Locate and identify every blood parasite.
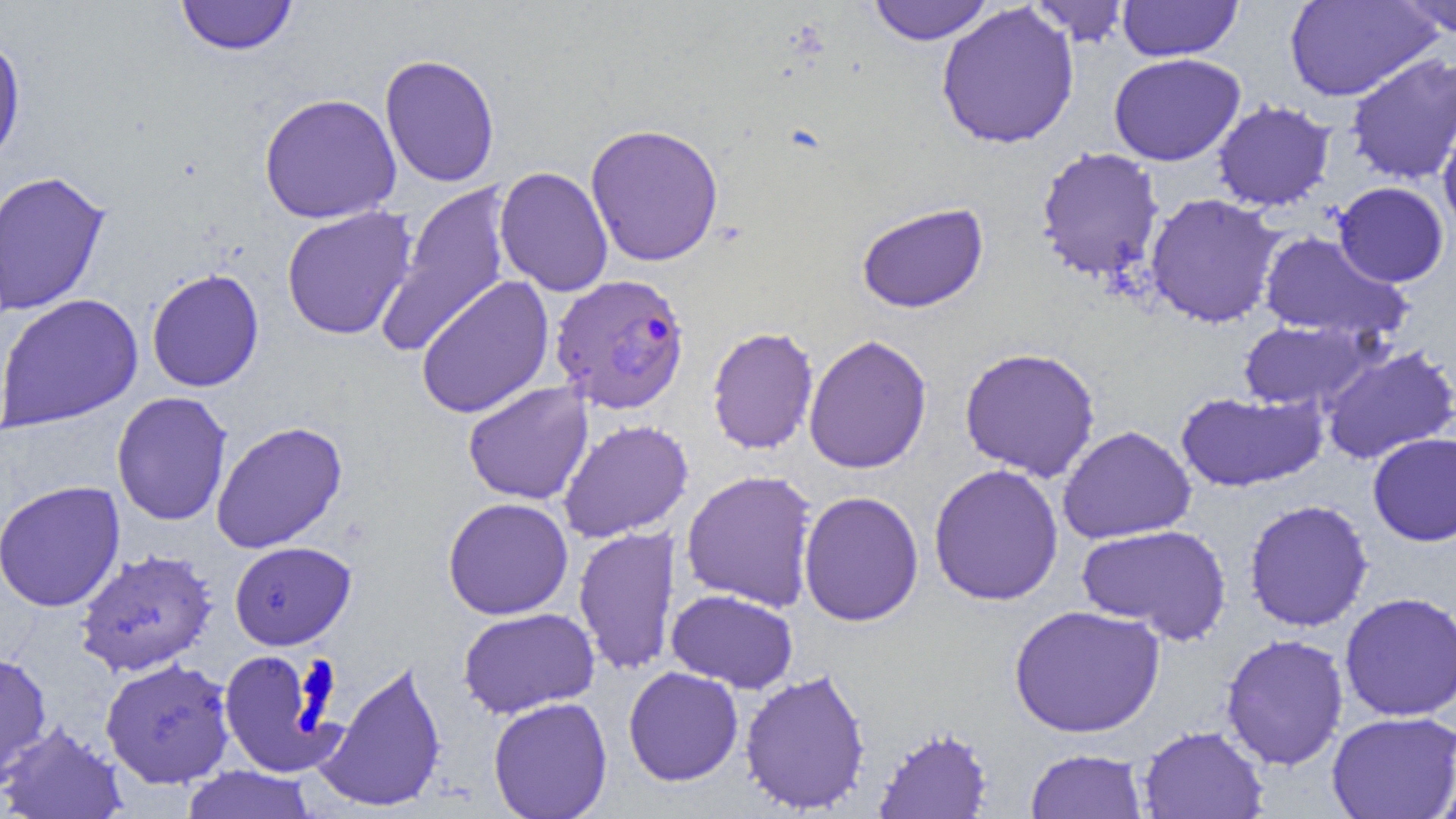
Approximate bounding boxes as named x1/y1/x2/y2 corners in pixels.
Plasmodium falciparum-infected red blood cells: (x1=549, y1=273, x2=690, y2=415).
No Plasmodium ovale, Plasmodium malariae, Plasmodium vivax, Babesia divergens, or Trypanosoma brucei observed.

Uninfected red blood cell locations: (x1=175, y1=0, x2=297, y2=56), (x1=1027, y1=0, x2=1132, y2=46), (x1=1285, y1=0, x2=1441, y2=102), (x1=1396, y1=0, x2=1456, y2=38), (x1=867, y1=1, x2=994, y2=45), (x1=1117, y1=1, x2=1242, y2=61), (x1=935, y1=3, x2=1080, y2=150), (x1=0, y1=33, x2=26, y2=169), (x1=1345, y1=52, x2=1456, y2=186), (x1=379, y1=53, x2=501, y2=187), (x1=1108, y1=53, x2=1245, y2=166), (x1=259, y1=92, x2=402, y2=225), (x1=1212, y1=101, x2=1335, y2=212), (x1=1437, y1=108, x2=1455, y2=239), (x1=585, y1=123, x2=724, y2=267), (x1=1035, y1=147, x2=1165, y2=282), (x1=495, y1=165, x2=614, y2=297), (x1=0, y1=169, x2=112, y2=317), (x1=379, y1=181, x2=513, y2=357), (x1=1333, y1=181, x2=1449, y2=287), (x1=1145, y1=193, x2=1284, y2=328), (x1=856, y1=202, x2=989, y2=314), (x1=280, y1=206, x2=418, y2=341), (x1=1257, y1=231, x2=1411, y2=342), (x1=146, y1=268, x2=265, y2=392), (x1=415, y1=274, x2=555, y2=420), (x1=0, y1=293, x2=144, y2=432), (x1=1238, y1=319, x2=1377, y2=411), (x1=706, y1=326, x2=819, y2=455), (x1=802, y1=334, x2=933, y2=474), (x1=1319, y1=345, x2=1456, y2=465), (x1=959, y1=347, x2=1101, y2=482), (x1=462, y1=381, x2=593, y2=505), (x1=1175, y1=390, x2=1328, y2=493), (x1=112, y1=392, x2=232, y2=526), (x1=558, y1=419, x2=694, y2=542), (x1=211, y1=421, x2=348, y2=553), (x1=1057, y1=425, x2=1196, y2=544), (x1=1367, y1=432, x2=1456, y2=546), (x1=928, y1=463, x2=1064, y2=606), (x1=681, y1=469, x2=819, y2=611), (x1=0, y1=480, x2=126, y2=612), (x1=798, y1=490, x2=924, y2=627), (x1=442, y1=497, x2=574, y2=620), (x1=1243, y1=499, x2=1374, y2=632), (x1=1076, y1=524, x2=1232, y2=645), (x1=573, y1=526, x2=681, y2=677), (x1=230, y1=541, x2=355, y2=650), (x1=74, y1=548, x2=218, y2=676), (x1=666, y1=589, x2=799, y2=693), (x1=1339, y1=591, x2=1456, y2=722), (x1=1008, y1=604, x2=1166, y2=738), (x1=458, y1=607, x2=599, y2=719), (x1=1220, y1=633, x2=1350, y2=770), (x1=217, y1=649, x2=341, y2=778), (x1=0, y1=650, x2=52, y2=785), (x1=100, y1=657, x2=236, y2=788), (x1=315, y1=658, x2=448, y2=813), (x1=623, y1=666, x2=744, y2=786), (x1=739, y1=667, x2=872, y2=815), (x1=488, y1=696, x2=613, y2=819), (x1=1326, y1=711, x2=1455, y2=819), (x1=0, y1=721, x2=127, y2=819), (x1=1138, y1=725, x2=1269, y2=819), (x1=873, y1=726, x2=994, y2=818), (x1=1025, y1=748, x2=1148, y2=819), (x1=180, y1=766, x2=317, y2=819). Slide-level diagnosis: Plasmodium falciparum. Image is 1456×819 pixels. Light microscopy. One field of a larger specimen. Thin blood film. 1000x magnification.